Classify this cell by malaria status.
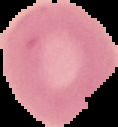

Uninfected.

image size = 118×127 pixels
preparation = thin blood smear
image type = segmented cell region on a black background